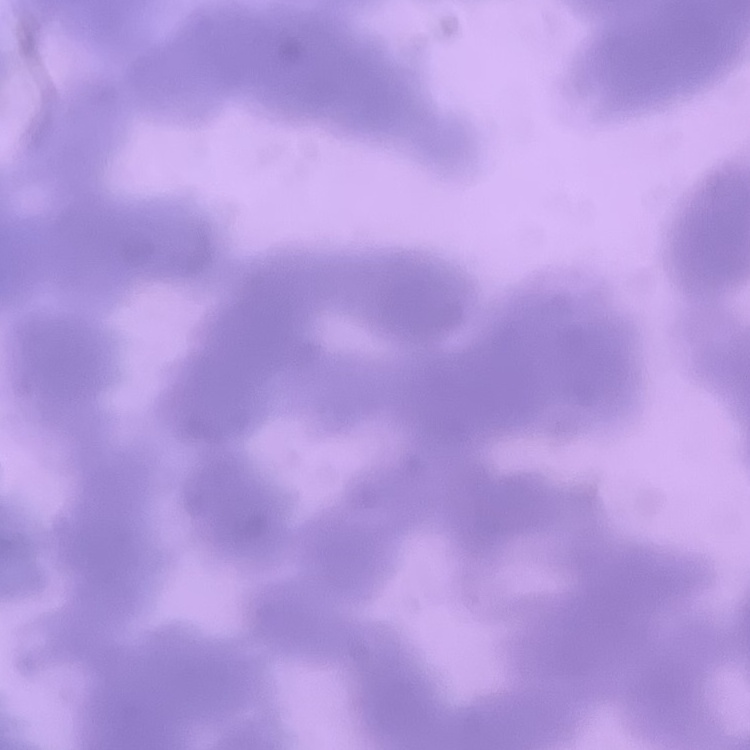

Summary:
  - Red blood cell morphology: rouleaux formation
  - Stain: Field's or Giemsa
  - Image type: one tile cut from a larger photomicrograph
  - Preparation: thin blood film